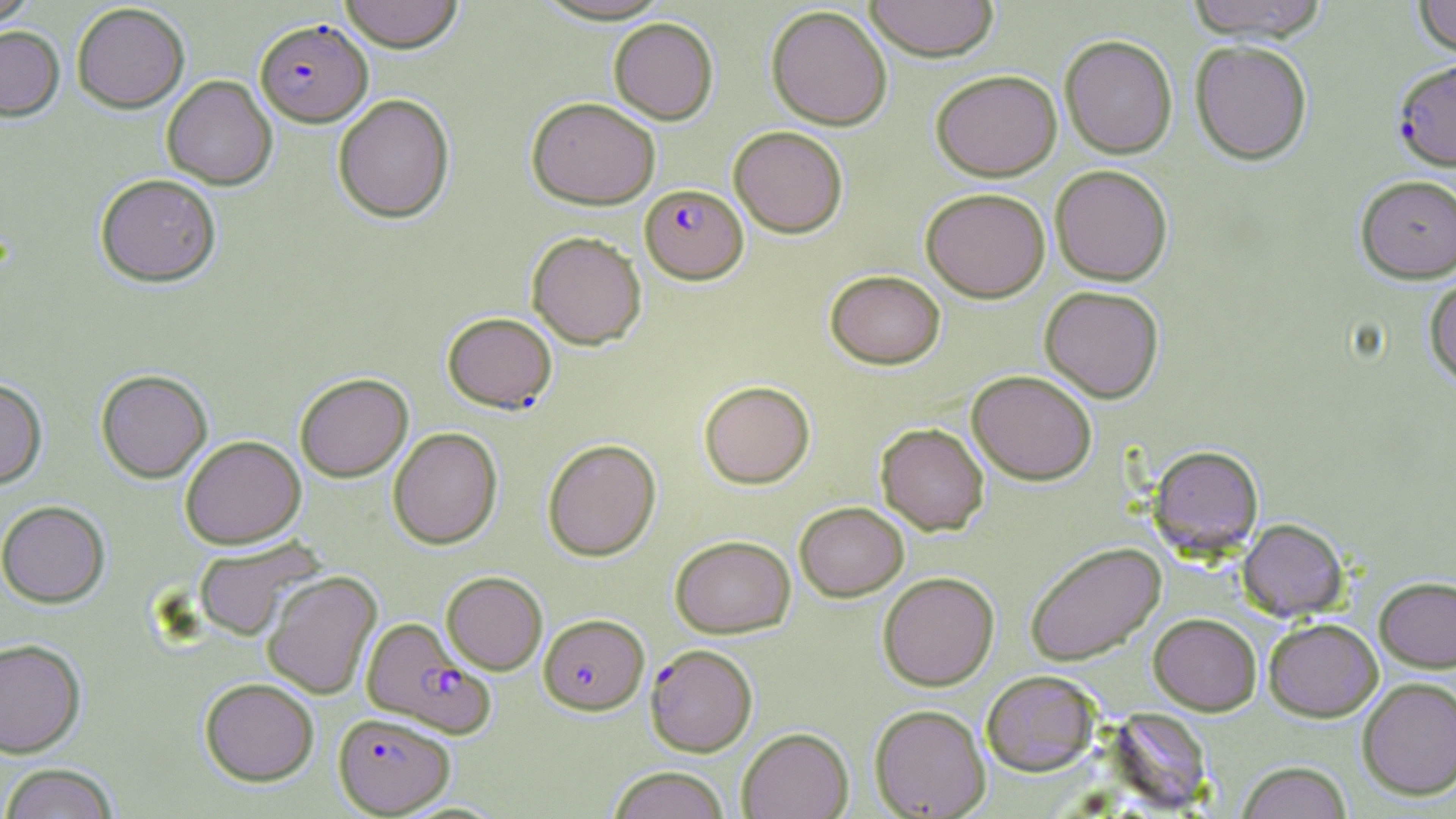
slide-level diagnosis = Plasmodium falciparum
modality = light microscopy
magnification = 1000x
uninfected red blood cell locations = approximate bounding boxes as named x1/y1/x2/y2 corners in pixels: (x1=0, y1=0, x2=40, y2=28), (x1=339, y1=0, x2=463, y2=52), (x1=864, y1=0, x2=999, y2=61), (x1=1185, y1=0, x2=1331, y2=41), (x1=1413, y1=0, x2=1456, y2=59), (x1=72, y1=3, x2=190, y2=112), (x1=766, y1=4, x2=892, y2=130), (x1=608, y1=17, x2=718, y2=124), (x1=0, y1=25, x2=65, y2=121), (x1=1059, y1=35, x2=1178, y2=159), (x1=1190, y1=40, x2=1313, y2=165), (x1=931, y1=69, x2=1062, y2=181), (x1=162, y1=75, x2=277, y2=190), (x1=333, y1=93, x2=455, y2=223), (x1=527, y1=96, x2=661, y2=209), (x1=729, y1=125, x2=848, y2=238), (x1=1050, y1=165, x2=1173, y2=285), (x1=95, y1=173, x2=221, y2=287), (x1=1355, y1=175, x2=1456, y2=283), (x1=921, y1=186, x2=1050, y2=302), (x1=526, y1=231, x2=647, y2=349), (x1=825, y1=269, x2=945, y2=369), (x1=1424, y1=274, x2=1456, y2=389), (x1=1039, y1=285, x2=1164, y2=403), (x1=442, y1=312, x2=557, y2=413), (x1=96, y1=369, x2=212, y2=483), (x1=967, y1=369, x2=1097, y2=485), (x1=295, y1=373, x2=413, y2=482), (x1=0, y1=378, x2=47, y2=489), (x1=699, y1=380, x2=815, y2=488), (x1=875, y1=422, x2=989, y2=535), (x1=388, y1=427, x2=503, y2=549), (x1=180, y1=435, x2=306, y2=548), (x1=542, y1=439, x2=661, y2=561), (x1=1148, y1=444, x2=1264, y2=558), (x1=0, y1=500, x2=110, y2=607), (x1=794, y1=501, x2=909, y2=601), (x1=1237, y1=518, x2=1348, y2=621), (x1=670, y1=535, x2=796, y2=638), (x1=192, y1=536, x2=325, y2=640), (x1=1025, y1=542, x2=1166, y2=666), (x1=262, y1=570, x2=382, y2=700), (x1=441, y1=571, x2=547, y2=674), (x1=878, y1=572, x2=999, y2=690), (x1=1374, y1=575, x2=1456, y2=672), (x1=1148, y1=613, x2=1262, y2=715), (x1=1263, y1=617, x2=1383, y2=721), (x1=0, y1=638, x2=86, y2=758), (x1=981, y1=670, x2=1102, y2=776), (x1=200, y1=677, x2=319, y2=785), (x1=1357, y1=677, x2=1456, y2=800), (x1=869, y1=704, x2=990, y2=818), (x1=737, y1=727, x2=854, y2=818), (x1=1236, y1=761, x2=1352, y2=819), (x1=0, y1=763, x2=120, y2=819), (x1=606, y1=766, x2=731, y2=819)
Plasmodium falciparum-infected red blood cell locations = approximate bounding boxes as named x1/y1/x2/y2 corners in pixels: (x1=255, y1=18, x2=372, y2=126), (x1=1393, y1=58, x2=1456, y2=171), (x1=640, y1=184, x2=748, y2=284), (x1=538, y1=613, x2=649, y2=715), (x1=360, y1=617, x2=495, y2=737), (x1=645, y1=643, x2=757, y2=757), (x1=333, y1=712, x2=456, y2=816)
stain = May-Grünwald-Giemsa
preparation = thin blood smear
field of view = one of a larger specimen
image size = 1456×819 pixels